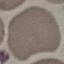

Malaria status: uninfected. Acquired by smartphone through the microscope eyepiece. Thin smear of blood. Giemsa stain. Automatically extracted cell patch, resized to 64 × 64 pixels.